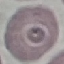 Malaria status: uninfected. Photographed with a smartphone camera at the microscope eyepiece. Cell patch, automatically extracted from a larger field of view and resized to 64 × 64 pixels. Thin blood smear. Giemsa-stained preparation.